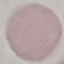
Result: no malaria parasites seen. Cell patch, automatically extracted from a larger field of view and resized to 64 × 64 pixels. Thin blood film. Giemsa-stained preparation. Photographed with a smartphone camera at the microscope eyepiece.